Outline each blood parasite and name the species.
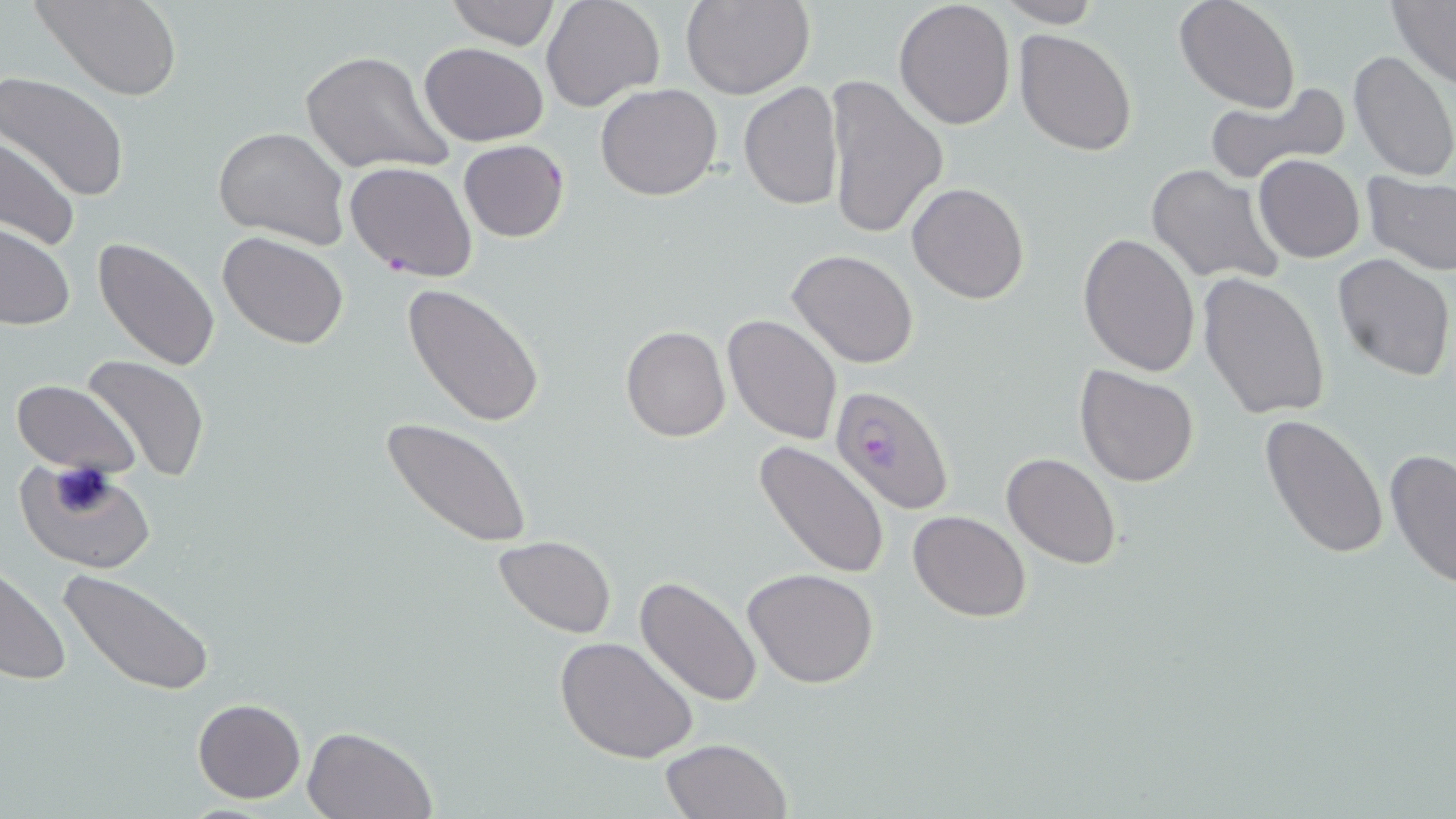
Approximate bounding boxes as (x1, y1, x2, y2) in pixels.
Plasmodium falciparum-infected red blood cells: (830, 386, 955, 515).
No Plasmodium ovale, Plasmodium malariae, Plasmodium vivax, Babesia divergens, or Trypanosoma brucei observed.

Uninfected red blood cell locations: (34, 0, 182, 101), (445, 0, 562, 50), (541, 0, 666, 112), (682, 0, 814, 99), (894, 1, 1016, 133), (990, 1, 1103, 27), (1174, 1, 1300, 112), (1389, 2, 1456, 87), (1014, 28, 1139, 156), (419, 43, 549, 145), (1347, 49, 1456, 183), (301, 50, 451, 178), (0, 73, 130, 204), (822, 74, 948, 242), (1203, 80, 1351, 186), (738, 82, 843, 210), (595, 84, 724, 202), (212, 124, 351, 250), (0, 136, 80, 253), (460, 140, 569, 242), (1253, 154, 1365, 263), (344, 161, 477, 282), (1145, 162, 1287, 287), (1361, 172, 1456, 275), (907, 182, 1030, 303), (0, 224, 75, 332), (218, 231, 349, 349), (1078, 234, 1202, 377), (93, 237, 221, 373), (787, 248, 917, 368), (1332, 252, 1455, 381), (1197, 272, 1332, 419), (401, 283, 547, 429), (722, 314, 843, 444), (620, 325, 730, 442), (79, 353, 211, 483), (1075, 365, 1200, 486), (11, 379, 140, 476), (1260, 413, 1389, 559), (382, 416, 535, 549), (754, 439, 891, 578), (1384, 446, 1455, 589), (1002, 452, 1122, 569), (13, 457, 158, 575), (907, 510, 1033, 622), (494, 534, 617, 638), (0, 566, 72, 689), (742, 568, 880, 689), (59, 569, 214, 698), (635, 575, 763, 708), (555, 635, 699, 765), (193, 698, 307, 802), (303, 725, 436, 818), (659, 738, 792, 819). Slide-level diagnosis: Plasmodium falciparum. Captured at 1000x magnification. One field of a larger specimen. May-Grünwald-Giemsa-stained preparation. Thin blood film. Image is 1456×819 pixels. Light microscopy.